State which parasite is depicted.
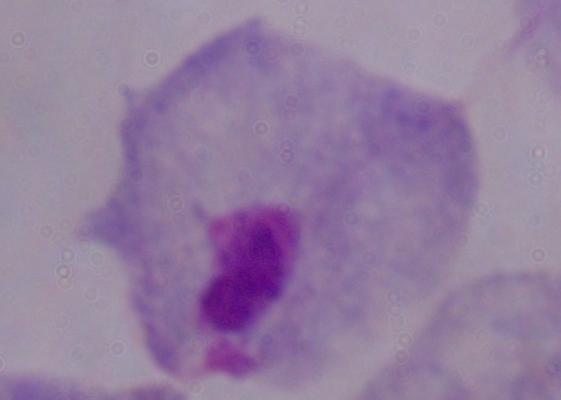
A trichomonad.

modality = micrograph
magnification = 1000x